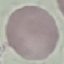
Malaria status: uninfected. Thin blood film. Automatically extracted cell patch, resized to 64 × 64 pixels. Photographed with a smartphone camera at the microscope eyepiece. Giemsa-stained preparation.